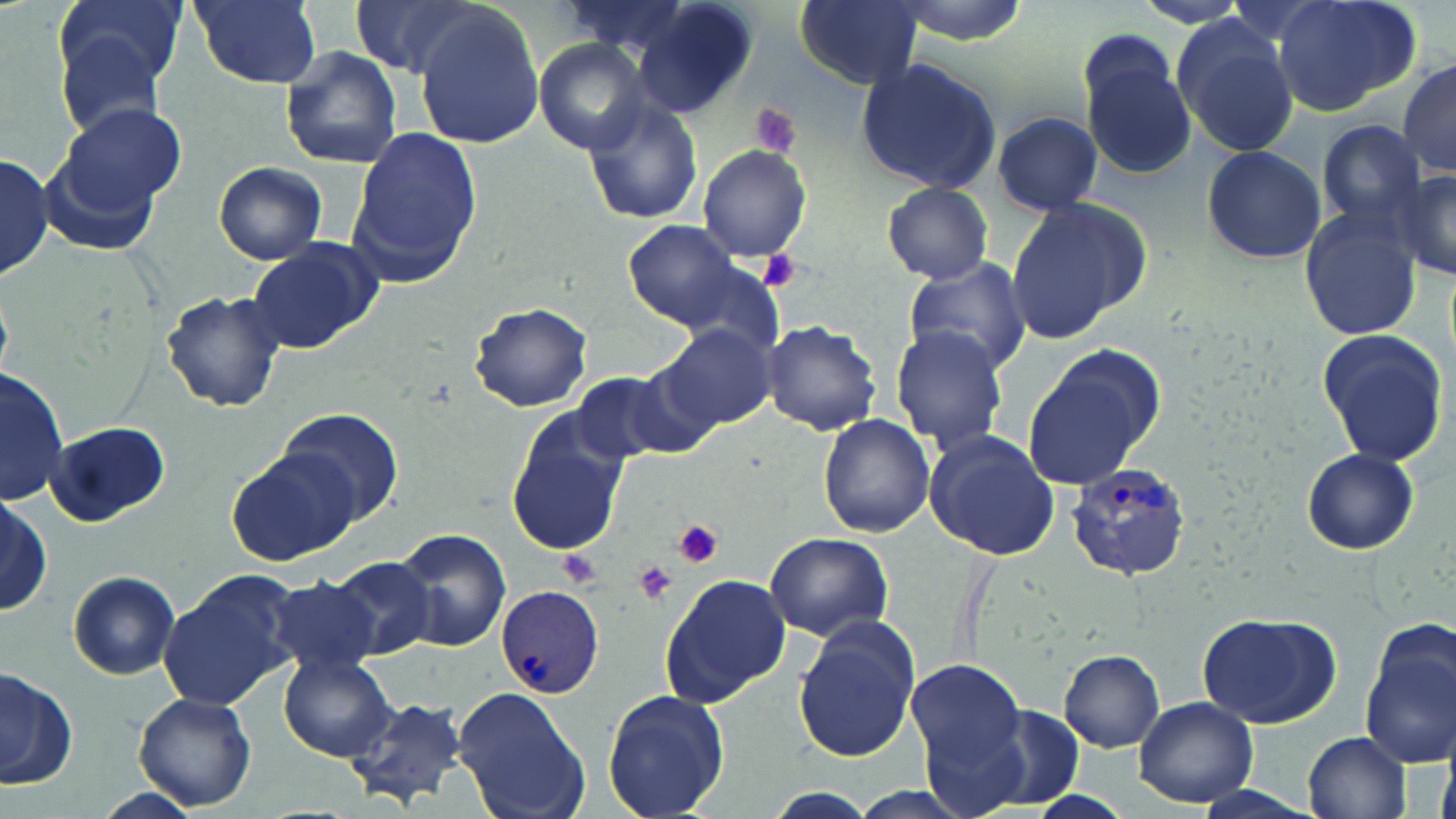

Approximate bounding boxes as (x1,y1)-(x2,y2) corner pairs in pixels. Uninfected red blood cell locations: (52,0)-(188,103), (186,0)-(324,91), (351,0)-(488,77), (561,0)-(694,59), (632,0)-(758,118), (796,0)-(924,89), (1272,1)-(1422,116), (413,10)-(546,148), (1174,24)-(1301,159), (54,32)-(172,145), (1078,33)-(1198,182), (535,39)-(652,154), (278,45)-(404,170), (855,59)-(1001,193), (1398,59)-(1456,176), (582,99)-(703,226), (54,103)-(188,221), (991,111)-(1103,216), (1316,119)-(1425,229), (347,128)-(481,285), (38,137)-(164,255), (698,144)-(812,263), (1201,144)-(1326,266), (0,153)-(51,282), (213,162)-(327,265), (1397,167)-(1456,278), (882,185)-(996,283), (1005,195)-(1147,345), (1297,207)-(1423,342), (626,221)-(739,326), (246,239)-(382,353), (903,257)-(1030,376), (678,261)-(787,357), (160,289)-(287,413), (469,301)-(593,413), (761,319)-(882,436), (658,323)-(777,432), (890,324)-(1013,455), (1316,330)-(1450,468), (1021,358)-(1157,491), (0,366)-(68,505), (574,368)-(710,464), (280,407)-(405,530), (818,413)-(936,538), (506,417)-(627,557), (46,421)-(171,525), (921,431)-(1059,561), (229,446)-(361,567), (1300,448)-(1420,555), (0,499)-(53,612), (396,530)-(511,653), (765,531)-(892,641), (328,555)-(436,661), (158,570)-(300,712), (660,570)-(791,705), (69,571)-(181,679), (264,578)-(383,680), (1196,612)-(1340,729), (791,615)-(922,763), (1360,625)-(1456,770), (1060,651)-(1164,753), (278,654)-(399,762), (903,658)-(1024,775), (0,665)-(77,793), (451,684)-(590,819), (602,688)-(729,818), (133,691)-(257,812), (344,692)-(471,809), (1134,696)-(1258,807), (979,705)-(1086,805), (920,713)-(1034,818), (1302,732)-(1411,818), (88,787)-(205,819), (750,789)-(891,819). Plasmodium vivax-infected red blood cell locations: (1064,461)-(1193,579), (496,584)-(605,698). Platelet locations: (745,101)-(805,163), (758,250)-(801,290), (671,518)-(724,568), (560,549)-(601,585), (636,559)-(678,603). Slide-level diagnosis: Plasmodium vivax. Optical microscopy. May-Grünwald-Giemsa stain. Captured at 1000x magnification. Image is 1456×819 pixels. Thin blood smear. Single field of view.